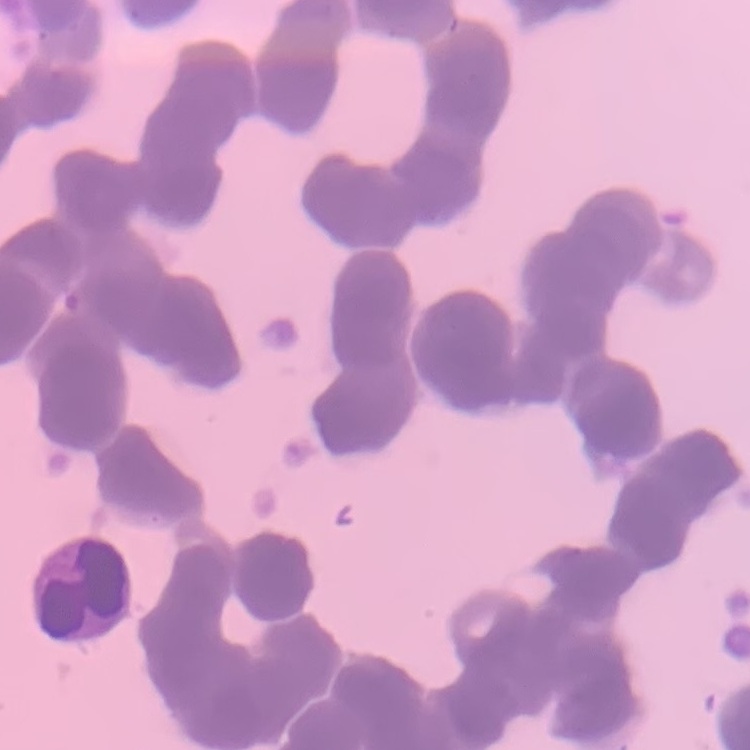

Summary:
  - Red blood cell morphology: rouleaux formation
  - Stain: Field's or Giemsa
  - Image type: square crop of a larger photomicrograph
  - Preparation: thin peripheral smear